Assess the morphology of the erythrocytes.
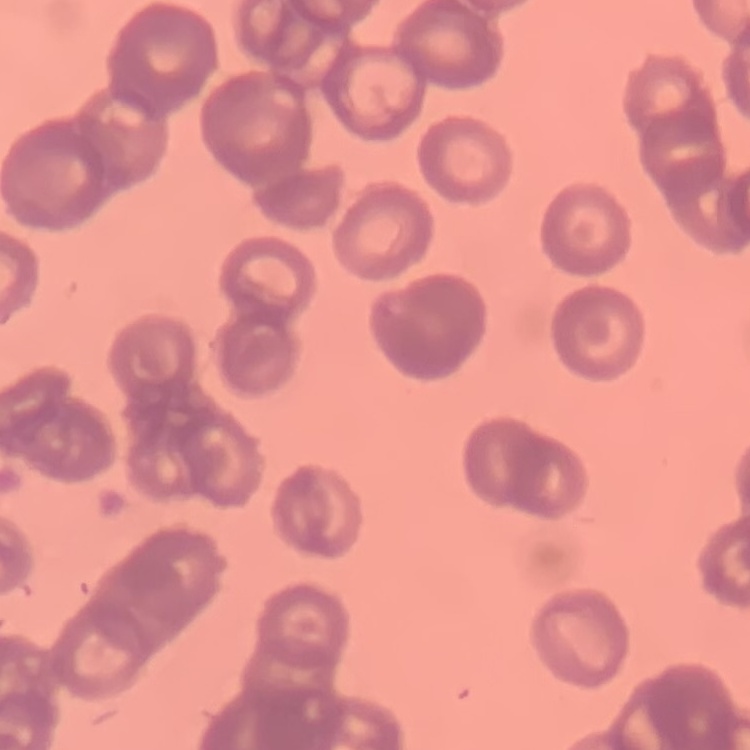
Rouleaux formation.

Thin blood film. One tile cut from a larger photomicrograph. Field's or Giemsa stain.